Give the extent of all uninfected red blood cells.
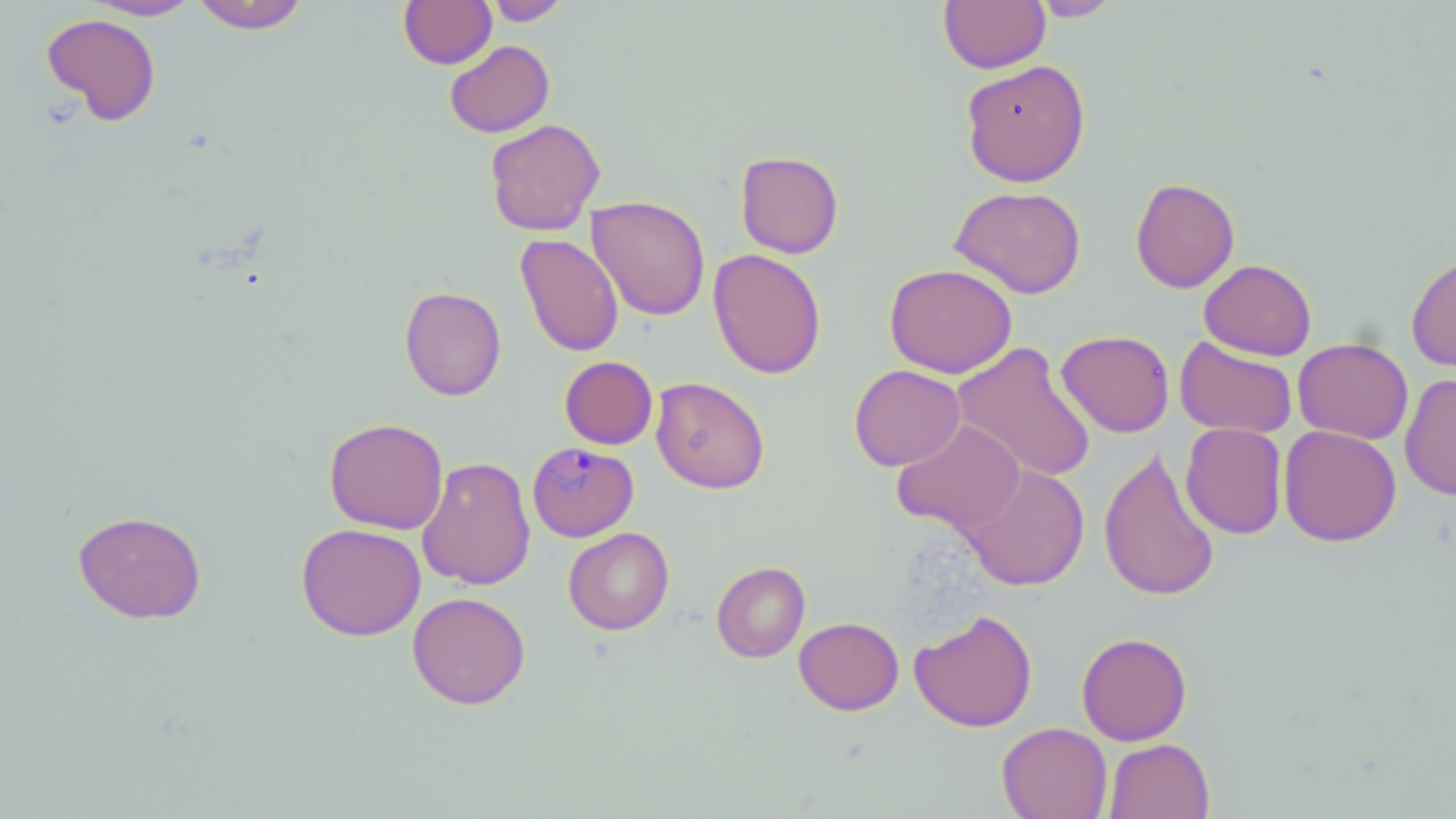

Approximate bounding boxes as (x1, y1, x2, y2) in pixels.
Uninfected red blood cells: (190, 0, 310, 34), (398, 0, 497, 68), (483, 0, 571, 26), (939, 0, 1050, 73), (1030, 0, 1122, 21), (86, 1, 201, 21), (42, 13, 161, 125), (444, 40, 555, 138), (961, 59, 1090, 187), (484, 118, 605, 236), (735, 150, 844, 258), (1130, 176, 1240, 293), (949, 185, 1087, 299), (587, 195, 710, 321), (515, 234, 624, 357), (708, 248, 827, 379), (1406, 254, 1456, 372), (1199, 259, 1317, 360), (884, 263, 1017, 378), (399, 285, 507, 401), (1056, 330, 1175, 437), (1174, 337, 1297, 439), (1293, 337, 1413, 444), (952, 341, 1096, 483), (559, 356, 658, 449), (849, 364, 965, 471), (1400, 374, 1456, 501), (650, 376, 770, 494), (324, 417, 448, 534), (892, 419, 1025, 533), (1181, 423, 1287, 539), (1279, 425, 1401, 546), (1098, 447, 1220, 602), (417, 457, 536, 590), (959, 463, 1090, 591), (73, 510, 207, 624), (296, 522, 426, 641), (563, 527, 674, 635), (712, 561, 810, 663), (407, 591, 530, 709), (909, 609, 1038, 733), (793, 616, 904, 715), (1076, 631, 1193, 745), (997, 722, 1112, 819), (1104, 738, 1214, 819).

Plasmodium malariae-infected red blood cell locations: (527, 442, 639, 542). Slide-level diagnosis: Plasmodium malariae. Thin blood film. Optical microscopy. 1000x magnification. Single field of view. Image is 1456×819 pixels. May-Grünwald-Giemsa stain.